Locate and identify every blood parasite.
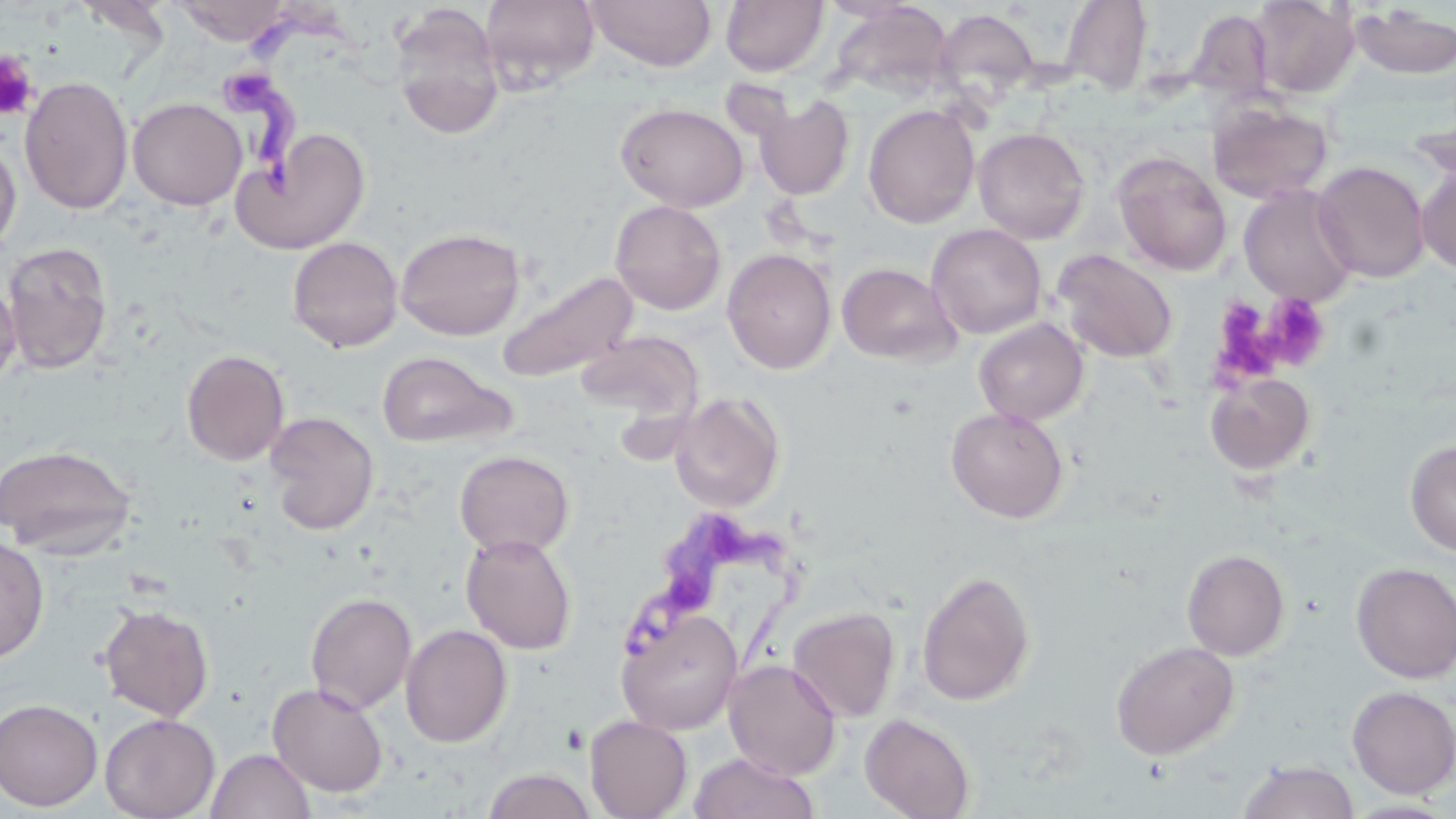

Approximate bounding boxes as (x1, y1, x2, y2) in pixels.
Trypanosoma brucei: (229, 0, 334, 200), (619, 522, 798, 680).
No Plasmodium falciparum, Plasmodium ovale, Plasmodium malariae, Plasmodium vivax, or Babesia divergens observed.

Platelet locations: (0, 51, 39, 121), (1261, 294, 1331, 373), (1212, 301, 1289, 384). Uninfected red blood cell locations: (173, 0, 292, 45), (479, 0, 600, 93), (584, 0, 716, 72), (721, 0, 828, 77), (1249, 0, 1359, 98), (1059, 1, 1154, 96), (389, 3, 505, 140), (1350, 5, 1456, 80), (934, 7, 1041, 103), (1187, 8, 1277, 105), (20, 74, 133, 215), (754, 95, 854, 200), (127, 97, 247, 210), (615, 102, 749, 212), (1207, 102, 1332, 204), (863, 103, 980, 228), (1407, 111, 1456, 187), (234, 127, 371, 254), (973, 127, 1090, 244), (0, 136, 21, 257), (1111, 150, 1232, 275), (1312, 161, 1430, 283), (1417, 164, 1456, 274), (1239, 186, 1357, 306), (610, 200, 726, 315), (926, 223, 1046, 339), (395, 227, 526, 340), (287, 236, 403, 354), (2, 241, 114, 375), (721, 248, 836, 375), (1052, 249, 1177, 364), (836, 262, 960, 365), (497, 269, 639, 384), (0, 274, 21, 390), (974, 318, 1089, 426), (577, 331, 703, 423), (181, 349, 290, 466), (376, 350, 514, 448), (1205, 372, 1316, 476), (669, 392, 785, 512), (946, 406, 1069, 523), (265, 411, 380, 535), (1405, 439, 1456, 557), (1, 443, 137, 558), (454, 450, 575, 558), (460, 532, 577, 655), (0, 535, 50, 662), (1182, 549, 1290, 660), (1351, 562, 1456, 684), (916, 569, 1036, 707), (305, 592, 417, 714), (98, 604, 214, 721), (787, 606, 901, 722), (616, 607, 743, 735), (400, 624, 512, 748), (1110, 641, 1239, 760), (723, 659, 841, 780), (267, 682, 389, 797), (1346, 686, 1456, 798), (0, 698, 103, 811), (100, 713, 220, 819), (860, 713, 976, 819), (584, 715, 692, 819), (206, 748, 315, 819), (689, 752, 819, 819), (1237, 759, 1360, 819), (482, 767, 597, 819), (1339, 798, 1456, 818). Slide-level diagnosis: Trypanosoma brucei. Single field of view. Image is 1456×819 pixels. Optical microscopy. 1000x magnification. May-Grünwald-Giemsa-stained preparation. Thin blood film.